Give the position of every malaria parasite.
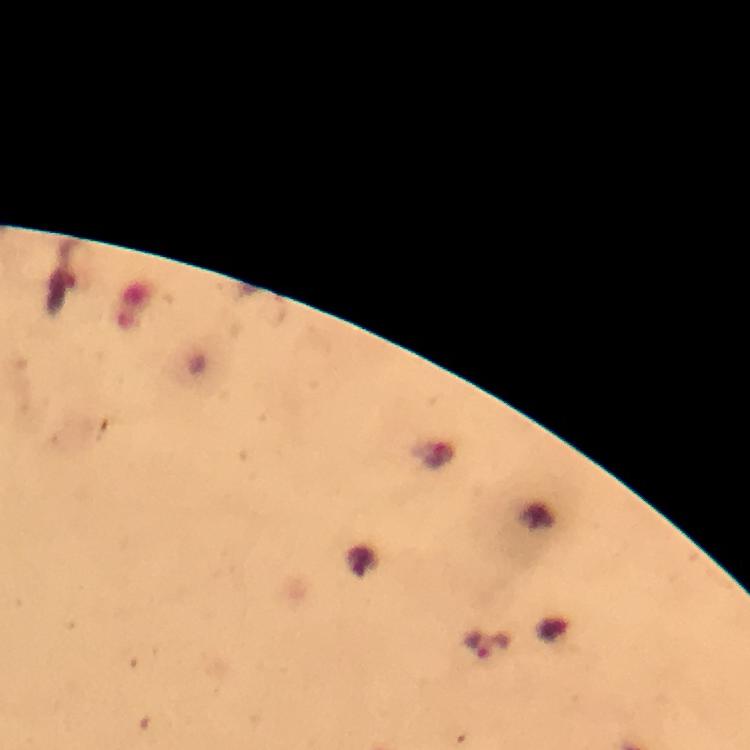

Approximate centers as {x, y} in pixels.
Malaria parasites: {492, 648}.

From a malaria diagnostic workup. Thick blood smear. Giemsa-stained preparation. At 100x magnification. Immersion oil applied. Photographed through the microscope with a smartphone camera. Image is 750×750 pixels. Cropped region of a single field of view.